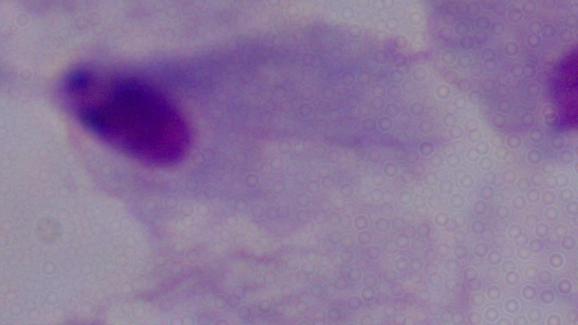

1000x magnification. Photomicrograph. A trichomonad is shown.